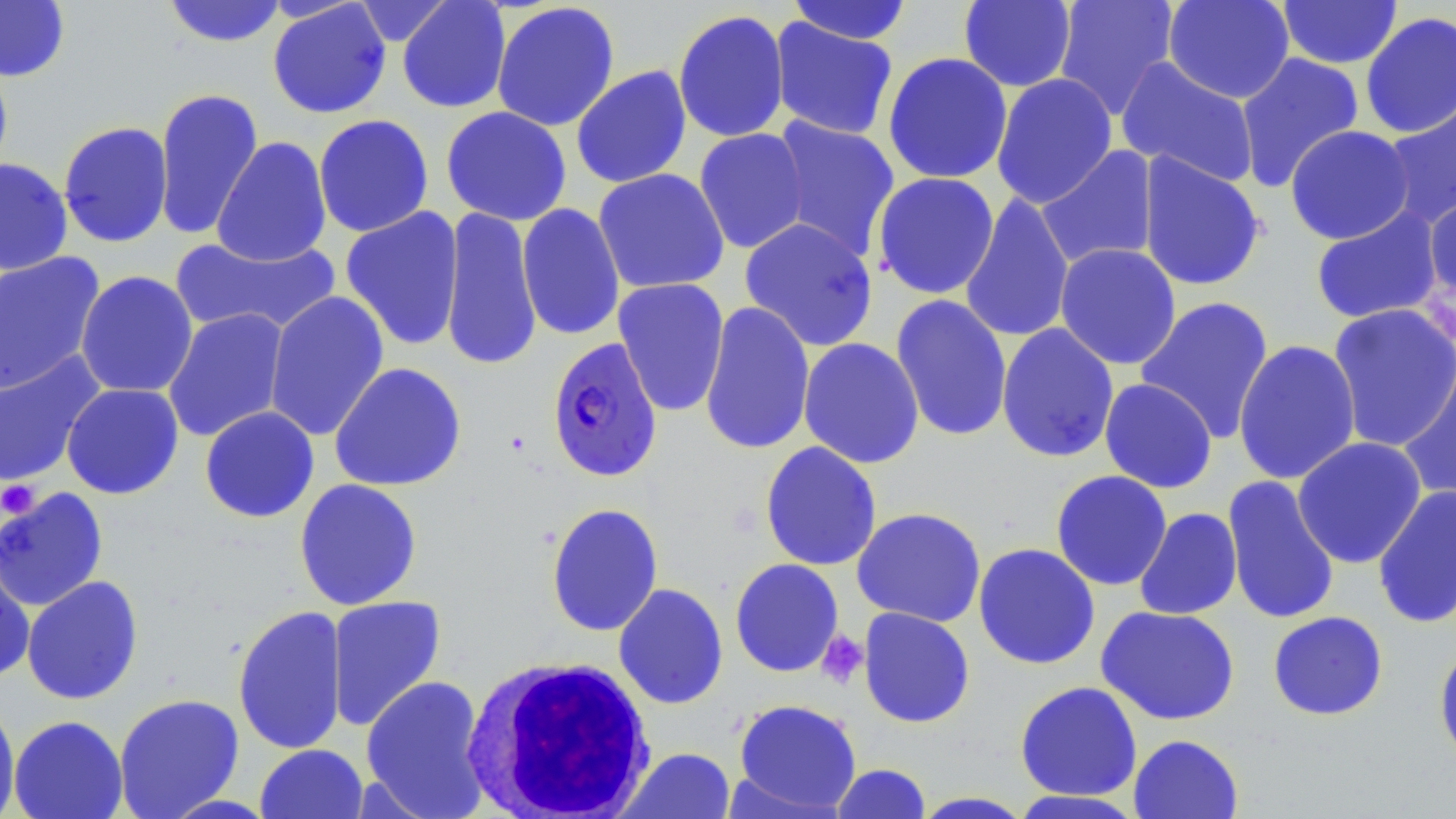

Approximate bounding boxes as (x1,y1)-(x2,y2) corner pairs in pixels. Platelet locations: (0,478)-(42,519), (816,630)-(869,689). Uninfected red blood cell locations: (0,0)-(69,82), (959,0)-(1077,92), (1163,0)-(1295,103), (1277,0)-(1403,69), (162,1)-(288,48), (268,1)-(391,119), (352,1)-(454,46), (397,1)-(511,113), (787,1)-(913,45), (1053,1)-(1179,119), (491,2)-(620,132), (673,9)-(790,143), (1360,10)-(1456,140), (768,17)-(899,140), (883,52)-(1013,184), (1235,52)-(1365,192), (1115,56)-(1260,188), (0,58)-(14,184), (571,65)-(692,189), (991,73)-(1118,209), (153,86)-(263,241), (1380,90)-(1456,230), (441,106)-(572,226), (313,114)-(434,238), (768,116)-(901,262), (58,121)-(174,248), (1284,124)-(1415,245), (694,127)-(810,254), (211,136)-(332,267), (1035,145)-(1159,270), (1137,152)-(1266,293), (0,158)-(73,275), (592,167)-(730,294), (872,172)-(1000,300), (959,192)-(1075,343), (1423,192)-(1456,307), (516,203)-(626,341), (439,205)-(542,372), (340,206)-(465,351), (1310,206)-(1444,326), (739,217)-(879,351), (171,234)-(341,338), (1054,243)-(1182,370), (0,251)-(107,396), (75,270)-(198,398), (612,277)-(730,417), (264,291)-(390,442), (890,294)-(1013,443), (1135,296)-(1275,442), (699,300)-(815,456), (1327,303)-(1456,452), (163,308)-(290,442), (996,323)-(1119,463), (798,337)-(924,469), (1233,339)-(1361,485), (0,352)-(106,487), (1396,353)-(1456,507), (329,362)-(467,492), (1099,378)-(1218,493), (61,383)-(184,499), (199,406)-(320,523), (1292,436)-(1427,569), (759,441)-(882,571), (1050,470)-(1173,591), (1222,475)-(1341,625), (294,478)-(423,610), (1372,484)-(1456,630), (0,487)-(109,612), (545,502)-(664,637), (851,507)-(986,627), (1134,507)-(1242,620), (973,542)-(1100,670), (0,550)-(36,683), (729,558)-(844,677), (21,575)-(144,705), (613,583)-(728,710), (326,595)-(447,732), (232,604)-(348,756), (1096,605)-(1241,726), (858,607)-(976,728), (1267,610)-(1388,721), (1433,640)-(1456,770), (360,675)-(491,817), (1014,680)-(1143,802), (113,693)-(244,818), (0,697)-(21,819), (733,698)-(862,815), (8,715)-(128,819), (1128,734)-(1244,819), (255,743)-(368,819), (616,747)-(737,819), (831,763)-(932,818), (1008,790)-(1147,819), (909,791)-(1035,818). Plasmodium falciparum-infected red blood cell locations: (546,337)-(663,483). White blood cell locations: (459,653)-(658,819). Slide-level diagnosis: Plasmodium falciparum. One field of a larger specimen. May-Grünwald-Giemsa-stained preparation. Light microscopy. Thin blood smear. Image is 1456×819 pixels. 1000x magnification.